Classify this cell by malaria status.
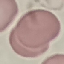
It is uninfected.

stain = Giemsa
capture = smartphone through the microscope eyepiece
image type = automatically extracted cell patch, resized to 64 × 64 pixels
preparation = thin blood smear